Report the malaria status of this cell.
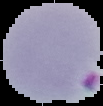
Parasitized.

image type = cell region segmented out of the field of view; surrounding area masked to black
preparation = thin blood film
image size = 103×106 pixels